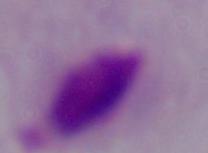
Micrograph. A trichomonad is shown. 1000x magnification.